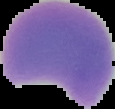
{
  "image_type": "segmented cell region with the area outside set to black",
  "preparation": "thin blood smear",
  "result": "no malaria parasites seen",
  "image_size": "115×109 pixels"
}